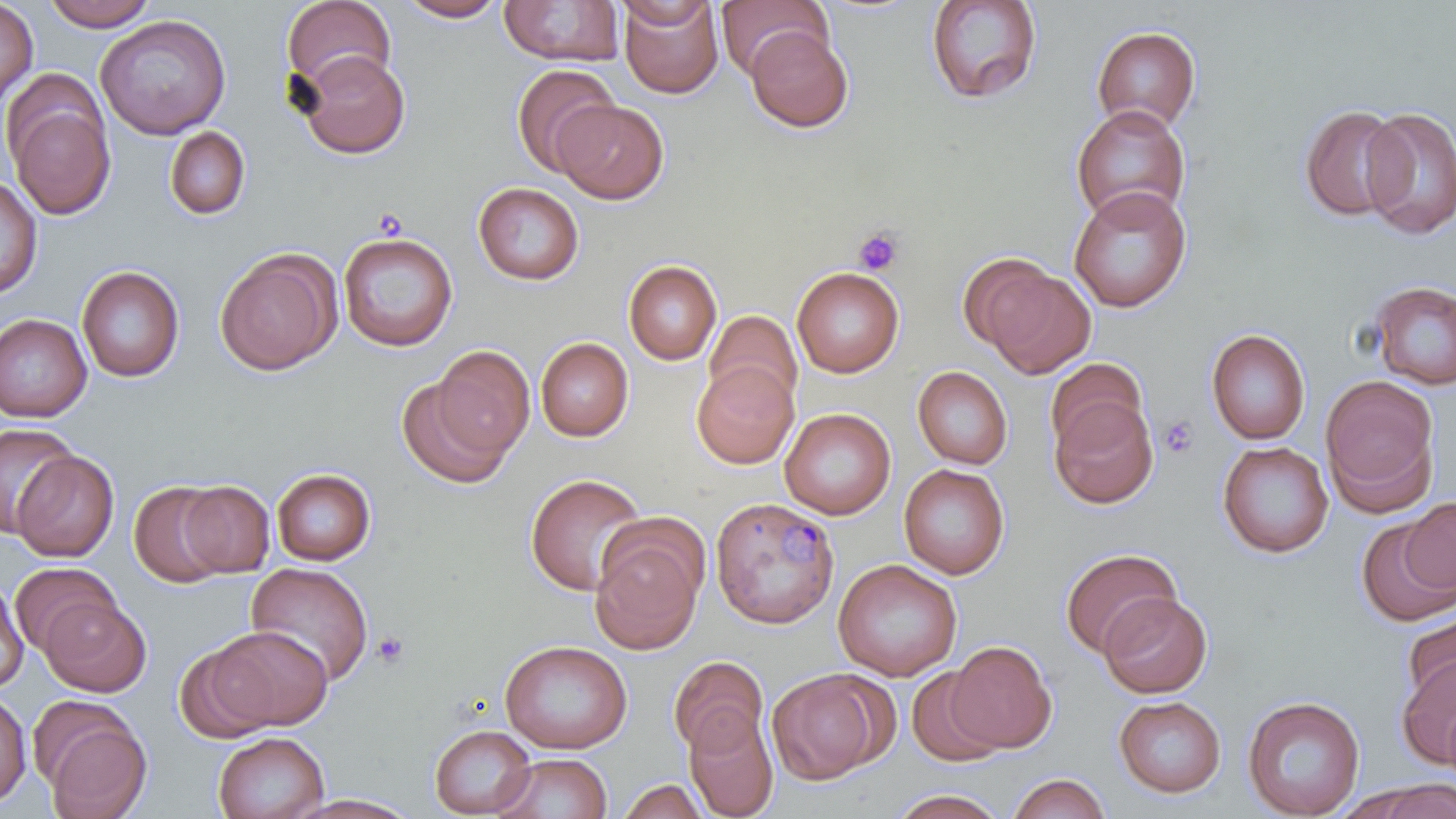

slide-level diagnosis = Plasmodium malariae
image size = 1456×819 pixels
platelet locations = approximate bounding boxes as [x1, y1, x2, y2] in pixels: [853, 226, 903, 275], [1158, 415, 1201, 459], [371, 631, 410, 670]
preparation = thin blood smear
modality = light microscopy
stain = May-Grünwald-Giemsa
uninfected red blood cell locations (subset) = approximate bounding boxes as [x1, y1, x2, y2] in pixels: [40, 0, 162, 30], [281, 0, 396, 95], [396, 0, 508, 22], [499, 0, 624, 66], [617, 0, 724, 98], [716, 0, 829, 80], [925, 0, 1042, 105], [0, 1, 38, 108], [613, 1, 718, 28], [94, 14, 231, 140], [1091, 25, 1201, 132], [746, 27, 853, 132], [298, 50, 410, 159], [512, 64, 620, 177], [4, 82, 116, 221], [553, 99, 669, 204], [1298, 103, 1406, 222], [1070, 104, 1191, 227], [1360, 106, 1456, 239], [164, 126, 251, 220], [0, 174, 42, 299], [473, 181, 584, 285], [1068, 186, 1192, 312], [338, 232, 458, 352], [214, 248, 342, 376], [623, 260, 722, 365], [978, 262, 1096, 378], [76, 265, 185, 383], [791, 267, 904, 378], [1368, 280, 1456, 389], [704, 309, 802, 410], [0, 314, 92, 422], [1205, 328, 1311, 445], [535, 337, 634, 442], [431, 344, 535, 461], [1045, 358, 1147, 454], [691, 361, 798, 469], [912, 366, 1013, 469], [1319, 374, 1439, 515], [395, 376, 515, 490], [1049, 397, 1158, 509], [780, 408, 896, 519], [1, 422, 77, 537], [1217, 441, 1333, 558], [11, 450, 119, 561], [898, 463, 1010, 579], [271, 468, 375, 566], [524, 472, 651, 596], [129, 481, 232, 588], [176, 481, 275, 577], [1400, 497, 1456, 595], [1355, 516, 1456, 626], [588, 523, 706, 656], [1059, 547, 1182, 658], [833, 559, 962, 681], [10, 562, 121, 657], [245, 562, 374, 687], [0, 578, 29, 692], [1098, 593, 1212, 698], [39, 595, 151, 697], [1402, 610, 1456, 709], [209, 626, 332, 731], [499, 639, 632, 754], [946, 640, 1056, 752], [175, 643, 276, 743], [667, 655, 768, 757], [1397, 656, 1456, 768], [905, 666, 1008, 767], [766, 668, 891, 784], [0, 692, 32, 808], [1242, 695, 1365, 818], [1113, 696, 1227, 798], [1443, 703, 1456, 787], [683, 708, 779, 819], [38, 709, 152, 819], [429, 724, 536, 817], [213, 731, 329, 819], [493, 753, 612, 819], [1007, 772, 1111, 819], [617, 778, 709, 819], [1370, 780, 1456, 819], [888, 788, 1008, 818], [289, 794, 421, 818]
field of view = single
magnification = 1000x